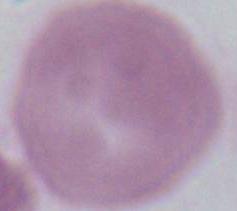 A red blood cell is seen. 1000x magnification. Photomicrograph.